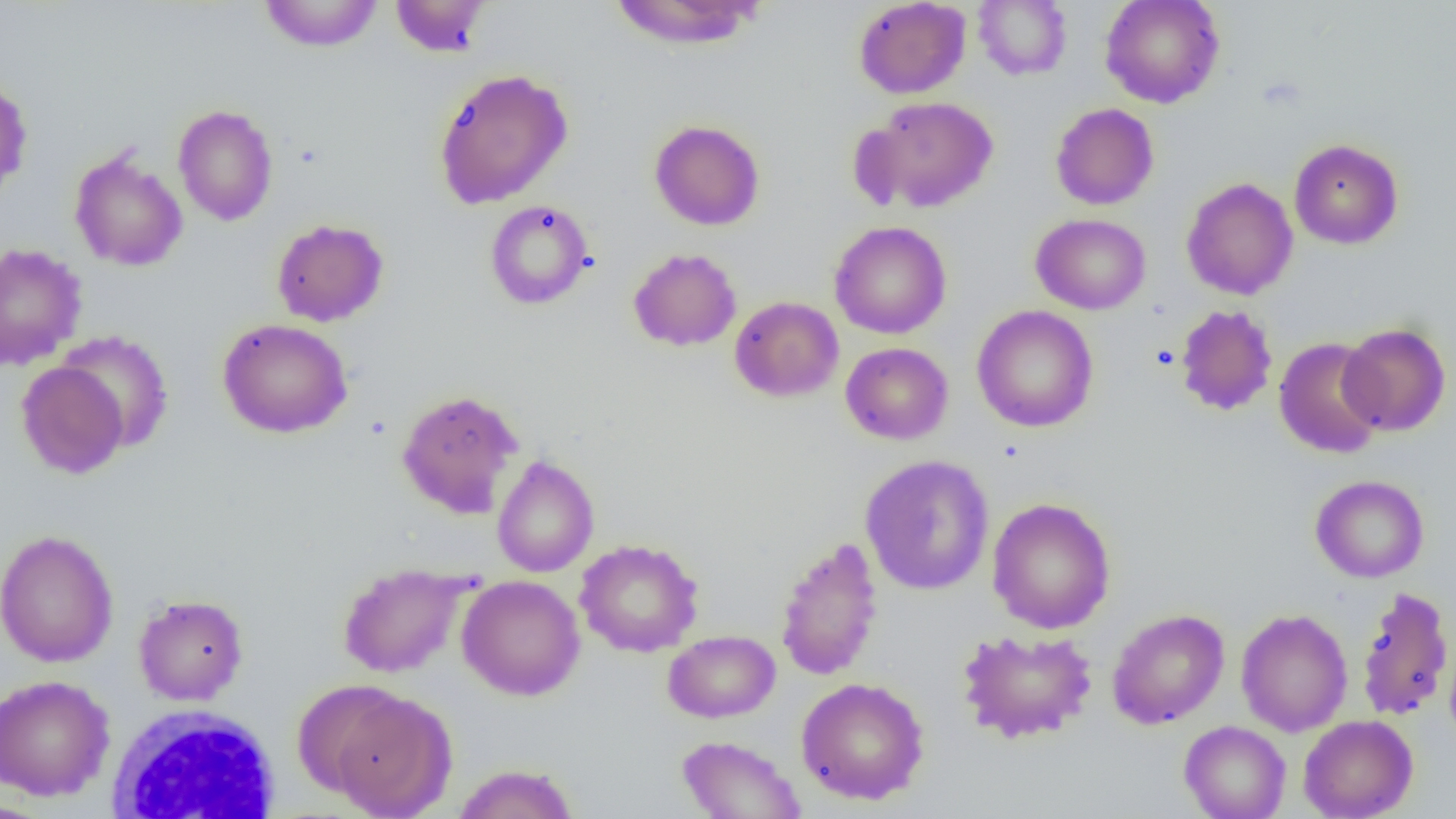
slide-level diagnosis = no evidence of blood parasites
uninfected red blood cell locations = approximate bounding boxes as [x1, y1, x2, y2] in pixels: [258, 0, 383, 52], [390, 0, 492, 57], [853, 0, 971, 99], [973, 0, 1072, 80], [1100, 0, 1225, 108], [607, 1, 765, 50], [432, 68, 574, 209], [0, 77, 33, 202], [863, 96, 998, 214], [1050, 103, 1159, 210], [173, 104, 279, 226], [649, 119, 765, 231], [1288, 139, 1403, 249], [69, 150, 188, 272], [1181, 177, 1298, 300], [484, 200, 594, 309], [1031, 213, 1151, 315], [271, 218, 389, 327], [829, 220, 951, 339], [0, 243, 87, 370], [628, 248, 741, 352], [730, 296, 844, 402], [1175, 304, 1278, 416], [972, 305, 1098, 432], [217, 318, 353, 439], [1338, 323, 1451, 436], [56, 330, 175, 452], [1274, 337, 1386, 459], [840, 342, 953, 445], [16, 361, 129, 479], [397, 389, 523, 517], [859, 454, 995, 595], [491, 455, 599, 577], [1310, 475, 1429, 582], [987, 497, 1116, 634], [0, 529, 119, 668], [775, 535, 883, 682], [575, 538, 704, 657], [337, 562, 472, 678], [456, 575, 586, 701], [1355, 585, 1454, 722], [133, 594, 249, 706], [1107, 608, 1229, 729], [1236, 608, 1353, 736], [956, 628, 1098, 744], [663, 631, 780, 722], [1445, 638, 1456, 750], [0, 674, 115, 802], [796, 677, 929, 805], [327, 688, 456, 817], [1299, 714, 1418, 819], [1179, 720, 1290, 819], [676, 735, 806, 819], [452, 763, 580, 819], [0, 800, 54, 819]
modality = light microscopy
magnification = 1000x
preparation = thin blood smear
image size = 1456×819 pixels
field of view = single
white blood cell locations = approximate bounding boxes as [x1, y1, x2, y2] in pixels: [105, 703, 282, 818]